Assess the morphology of the erythrocytes.
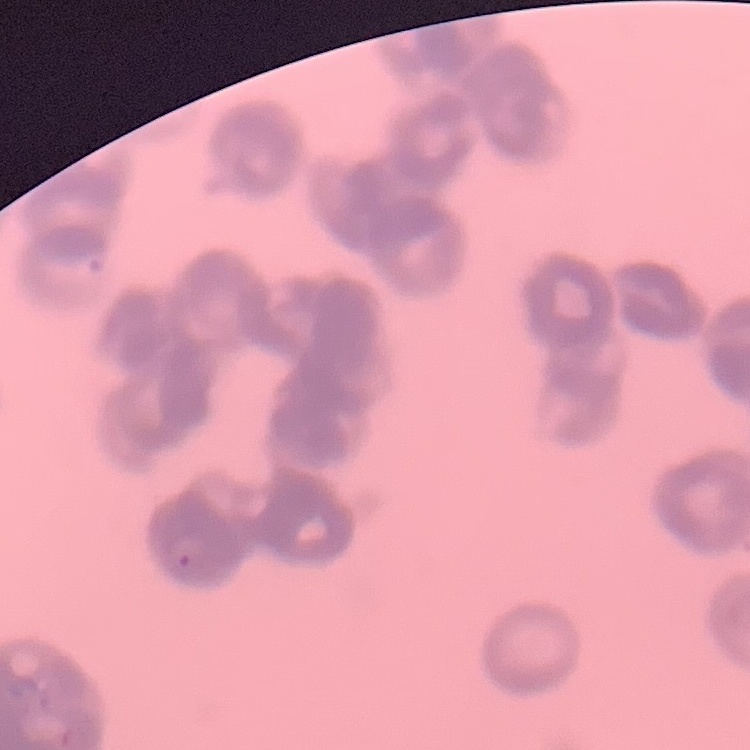

They show rouleaux formation.

preparation = thin blood film
image type = one tile cut from a larger photomicrograph
stain = Field's or Giemsa